Comment on the morphology of the erythrocytes.
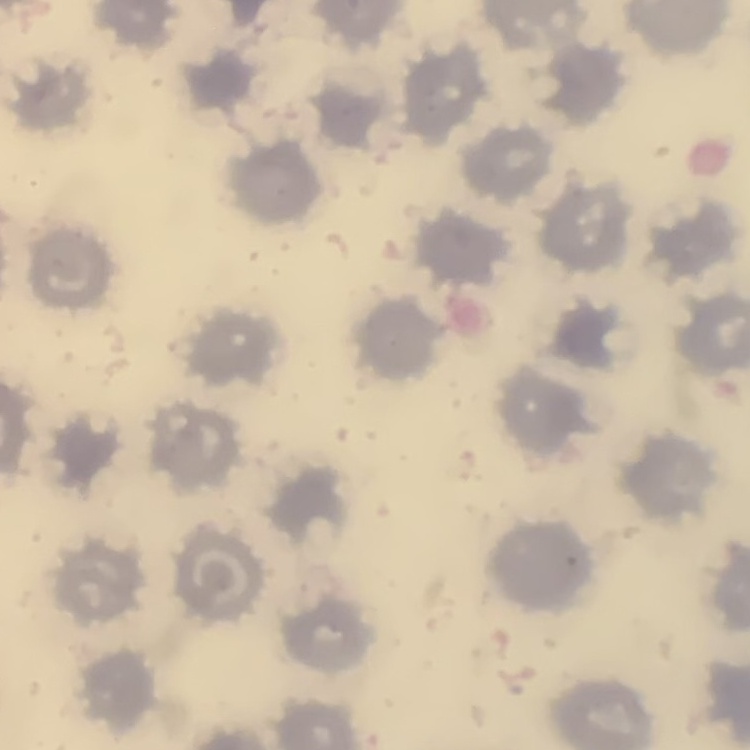
They show no rouleaux formation.

Thin blood film. One tile cut from a larger photomicrograph. Stained with either Field's or Giemsa.